Classify this cell by malaria status.
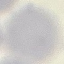

It is uninfected.

image_type: cell patch, automatically extracted from a larger field of view and resized to 64 × 64 pixels
preparation: thin blood film
stain: Giemsa
capture: smartphone through the microscope eyepiece